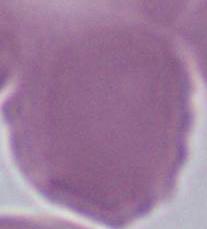
{
  "modality": "photomicrograph",
  "identification": "red blood cell",
  "magnification": "1000x"
}